Identify the parasite.
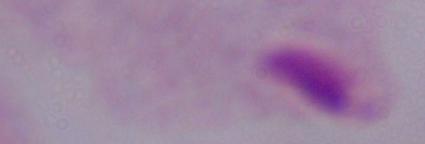

A trichomonad.

magnification = 1000x
modality = photomicrograph